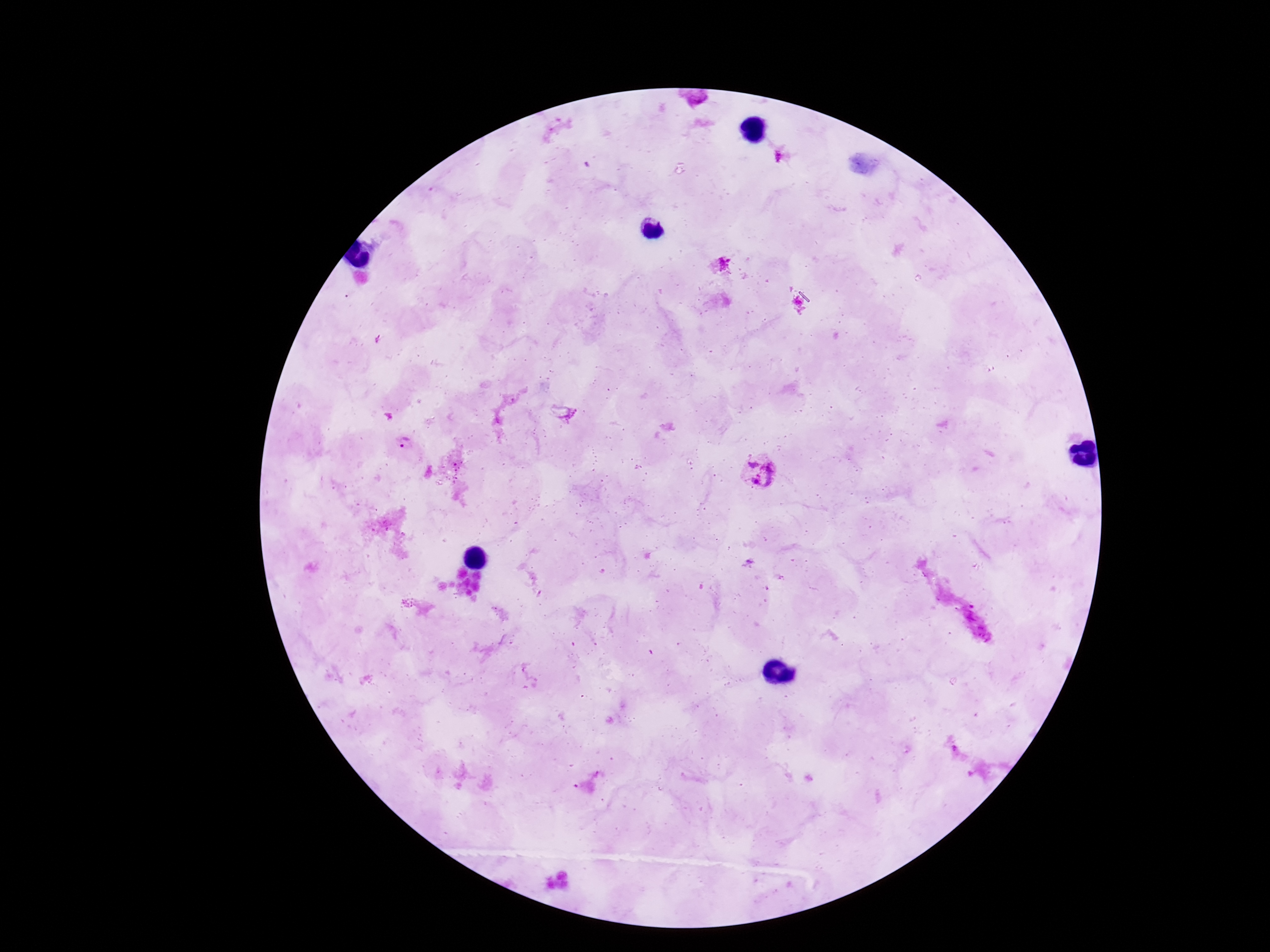

Approximate centers as (x, y) in pixels.
Summary:
  - Plasmodium parasite locations: (725, 263), (403, 444), (758, 473)
  - Image size: 1270×952 pixels
  - Magnification: 100x
  - Preparation: thick blood smear
  - Patient malaria status: positive
  - Capture: smartphone camera through the microscope eyepiece
  - Field of view: single
  - Stain: Giemsa